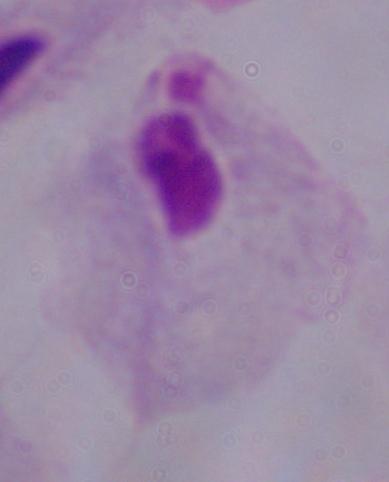

identification = trichomonad
modality = photomicrograph
magnification = 1000x